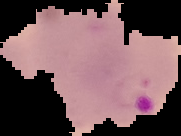

Image is 181×136 pixels. Result: Plasmodium parasites identified. From a thin blood film. Cell region segmented out of the field of view; the surrounding area is masked to black.